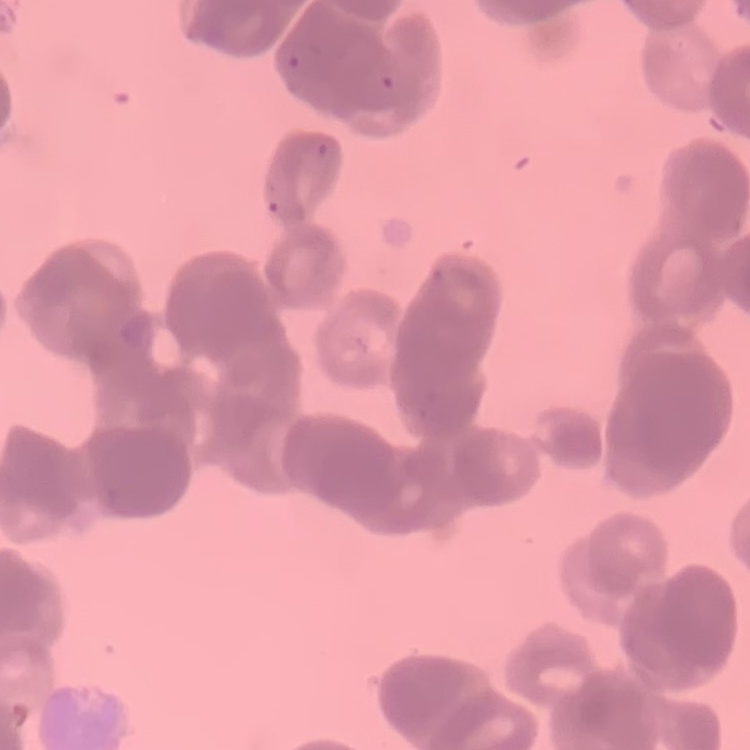
erythrocyte morphology = rouleaux formation
image type = one tile cut from a larger photomicrograph
preparation = thin blood smear
stain = Field's or Giemsa